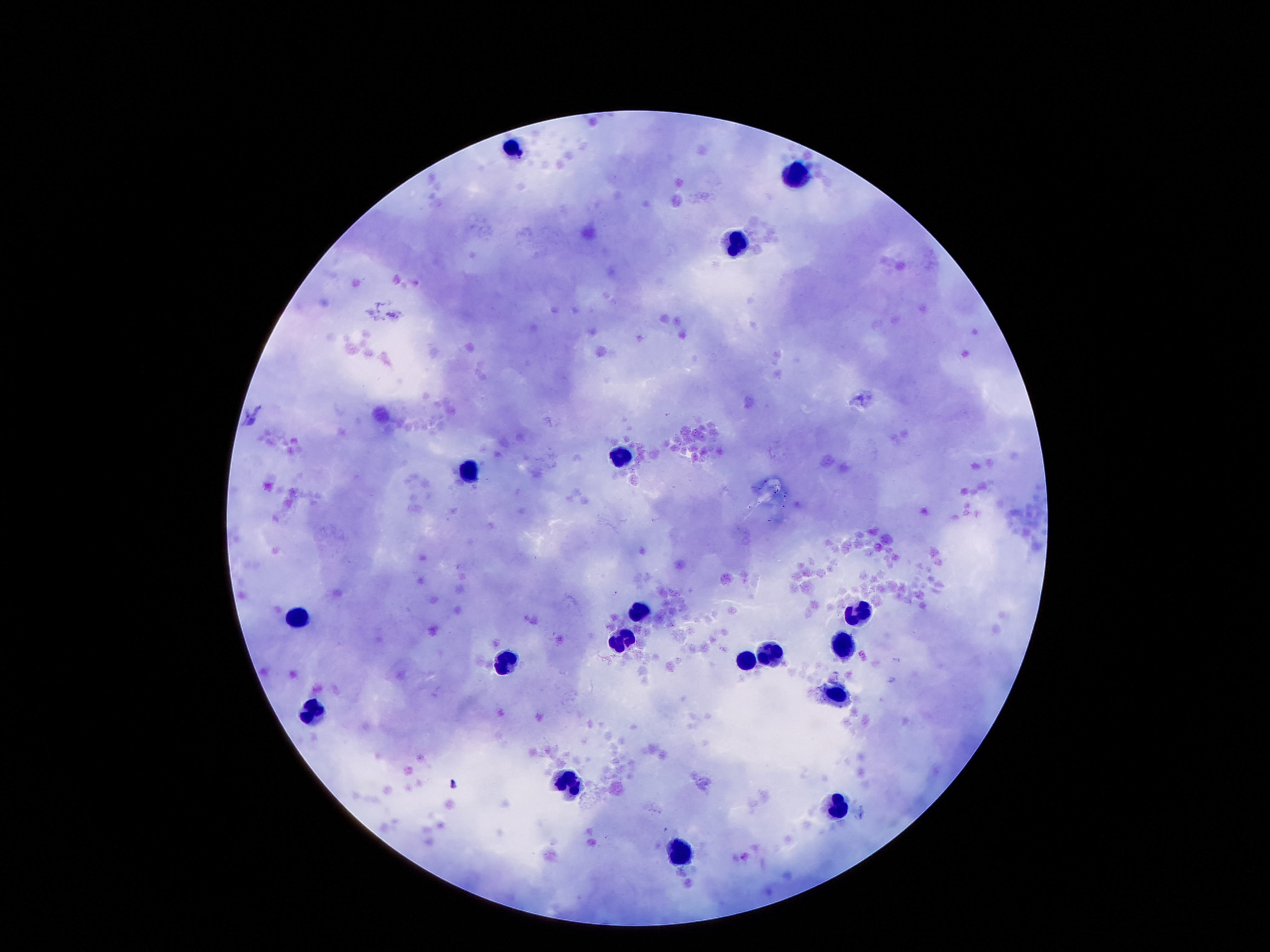

Approximate centers as (x, y) in pixels.
Summary:
  - Leukocyte locations: (514, 147), (795, 170), (736, 246), (621, 449), (467, 467), (635, 615), (859, 615), (297, 617), (623, 639), (844, 645), (775, 656), (744, 660), (508, 662), (840, 697), (316, 713), (568, 787), (840, 803), (680, 852)
  - Patient malaria status: negative
  - Image size: 1270×952 pixels
  - Field of view: one from this slide
  - Preparation: thick peripheral-blood smear
  - Stain: Giemsa
  - Capture: smartphone camera through the microscope eyepiece
  - Magnification: 100x